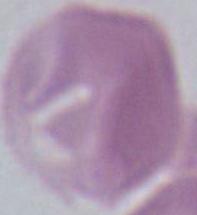

Micrograph. An erythrocyte is seen. Captured at 1000x magnification.